State which cell type is depicted.
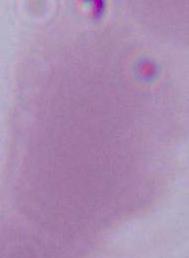
An erythrocyte.

{
  "magnification": "1000x",
  "modality": "micrograph"
}